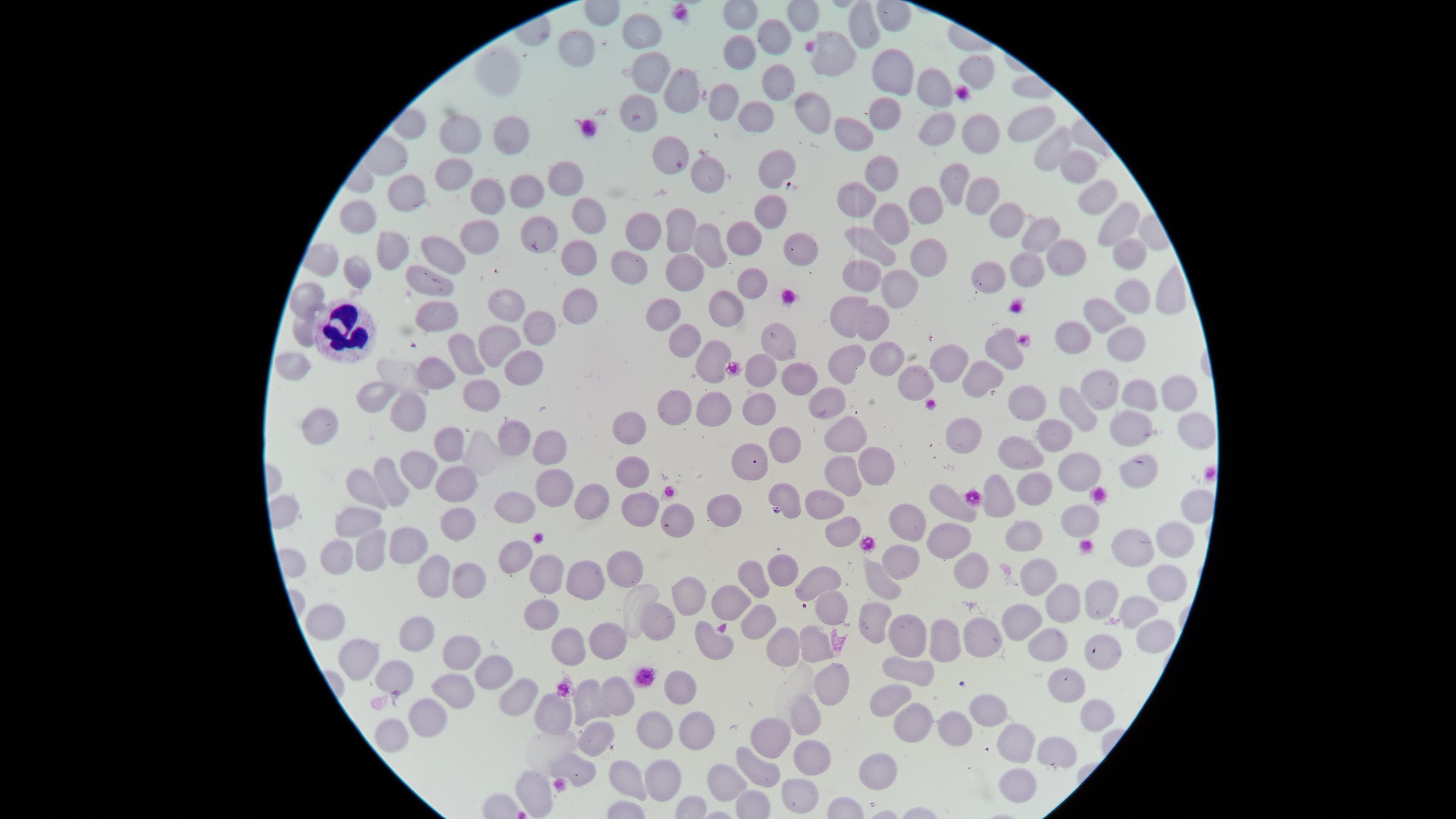

Approximate marker points as [x, y] in pixels.
Summary:
  - Uninfected red blood cells: [643, 29], [857, 31], [770, 41], [579, 49], [737, 56], [833, 59], [975, 69], [505, 76], [651, 78], [888, 78], [778, 82], [692, 85], [934, 87], [725, 104], [810, 109], [760, 112], [879, 116], [1025, 119], [938, 122], [643, 123], [465, 133], [972, 133], [514, 134], [858, 136], [672, 144], [1047, 149], [778, 164], [703, 169], [881, 173], [1071, 173], [455, 174], [564, 177], [953, 186], [522, 192], [409, 193], [487, 198], [982, 198], [855, 199], [926, 206], [1090, 206], [946, 207], [769, 212], [888, 215], [577, 217], [1008, 217], [362, 218], [1115, 221], [1042, 224], [476, 230], [678, 232], [641, 233], [541, 236], [746, 236], [707, 243], [875, 245], [392, 250], [442, 253], [800, 253], [921, 255], [1123, 256], [1058, 260], [584, 262], [621, 267], [362, 271], [1021, 272], [679, 276], [863, 279], [985, 280], [421, 282], [749, 282], [894, 283], [1164, 296], [298, 299], [503, 299], [1122, 300], [578, 303], [726, 311], [852, 312], [664, 314], [439, 315], [875, 318], [1103, 318], [540, 323], [303, 327], [1072, 332], [1119, 339], [507, 340], [681, 340], [774, 345], [1009, 352], [466, 353], [855, 356], [712, 357], [884, 358], [949, 363], [296, 369], [528, 371], [434, 374], [758, 379], [795, 380], [984, 380], [923, 381], [1100, 388], [1174, 392], [483, 393], [366, 395], [1142, 396], [1019, 398], [825, 401], [1073, 403], [675, 406], [712, 407], [764, 407], [405, 416], [1187, 423], [326, 429], [1120, 430], [633, 431], [451, 436], [1057, 436], [510, 440], [842, 441], [965, 441], [784, 442], [547, 443], [1024, 452], [752, 462], [876, 464], [414, 465], [630, 469], [1138, 470], [1078, 472], [835, 476], [389, 478], [451, 479], [551, 484], [1036, 484], [371, 492], [590, 494], [781, 499], [637, 500], [1000, 500], [951, 503], [824, 505], [512, 510], [725, 510], [1077, 517], [913, 518], [362, 520], [459, 521], [680, 521], [835, 528], [1021, 530], [954, 542], [1167, 542], [407, 545], [1121, 547], [373, 554], [518, 554], [335, 559], [625, 559], [896, 563], [782, 568], [1046, 569], [547, 572], [432, 573], [761, 573], [588, 574], [979, 575], [876, 579], [813, 580], [1158, 584], [466, 585], [1100, 595], [690, 596], [1061, 600], [728, 605], [1136, 612], [540, 613], [827, 615], [1018, 617], [756, 621], [875, 621], [658, 622], [338, 623], [992, 633], [412, 639], [607, 639], [1148, 639], [907, 641], [1045, 644], [706, 645], [571, 646], [781, 646], [936, 647], [1099, 647], [810, 650], [456, 653], [365, 656], [494, 674], [405, 676], [901, 676], [674, 685], [830, 686], [1062, 689], [448, 693], [521, 694], [618, 694], [590, 697], [887, 698], [989, 705], [558, 711], [1101, 712], [807, 714], [910, 717], [425, 719], [654, 724], [950, 733], [780, 734], [690, 737], [380, 739], [1017, 741], [593, 745], [1046, 745], [804, 757], [885, 762], [568, 769], [760, 770], [660, 779], [723, 780], [622, 781], [1005, 785], [537, 791], [792, 796]
  - White blood cells: [347, 332]
  - Presence: no malaria parasites identified
  - Capture: smartphone photograph through the microscope eyepiece
  - Stain: Giemsa
  - Preparation: thin blood film
  - Visible region: circular
  - Field of view: single
  - Image size: 1456×819 pixels